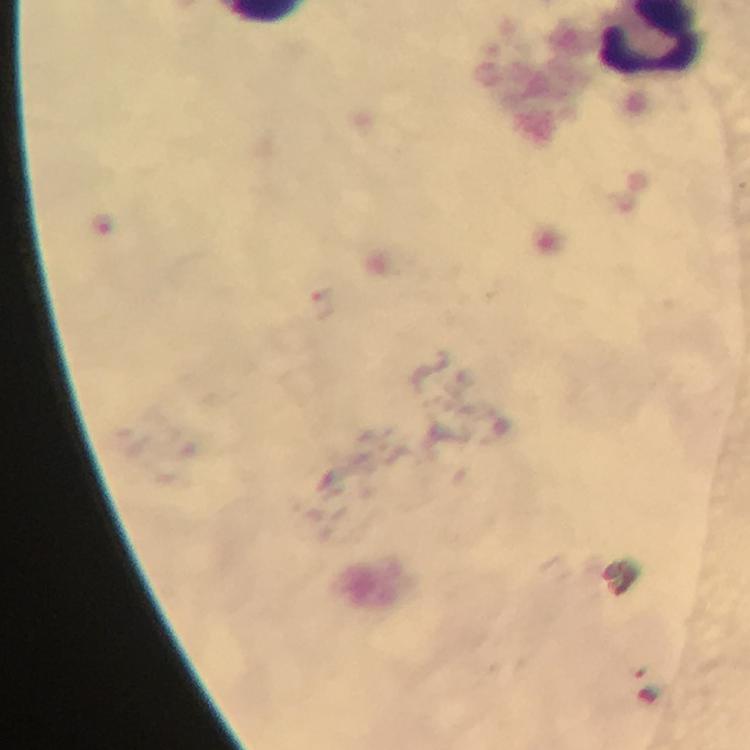 Approximate object centers, in pixels from the top-left corner. Malaria parasite locations: (x=102, y=221), (x=323, y=301). Cropped region of a single field of view. Giemsa-stained preparation. Image is 750×750 pixels. Smartphone photograph taken through a microscope. From a diagnostic examination for malaria. Immersion oil was used. 100x magnification. Thick smear.